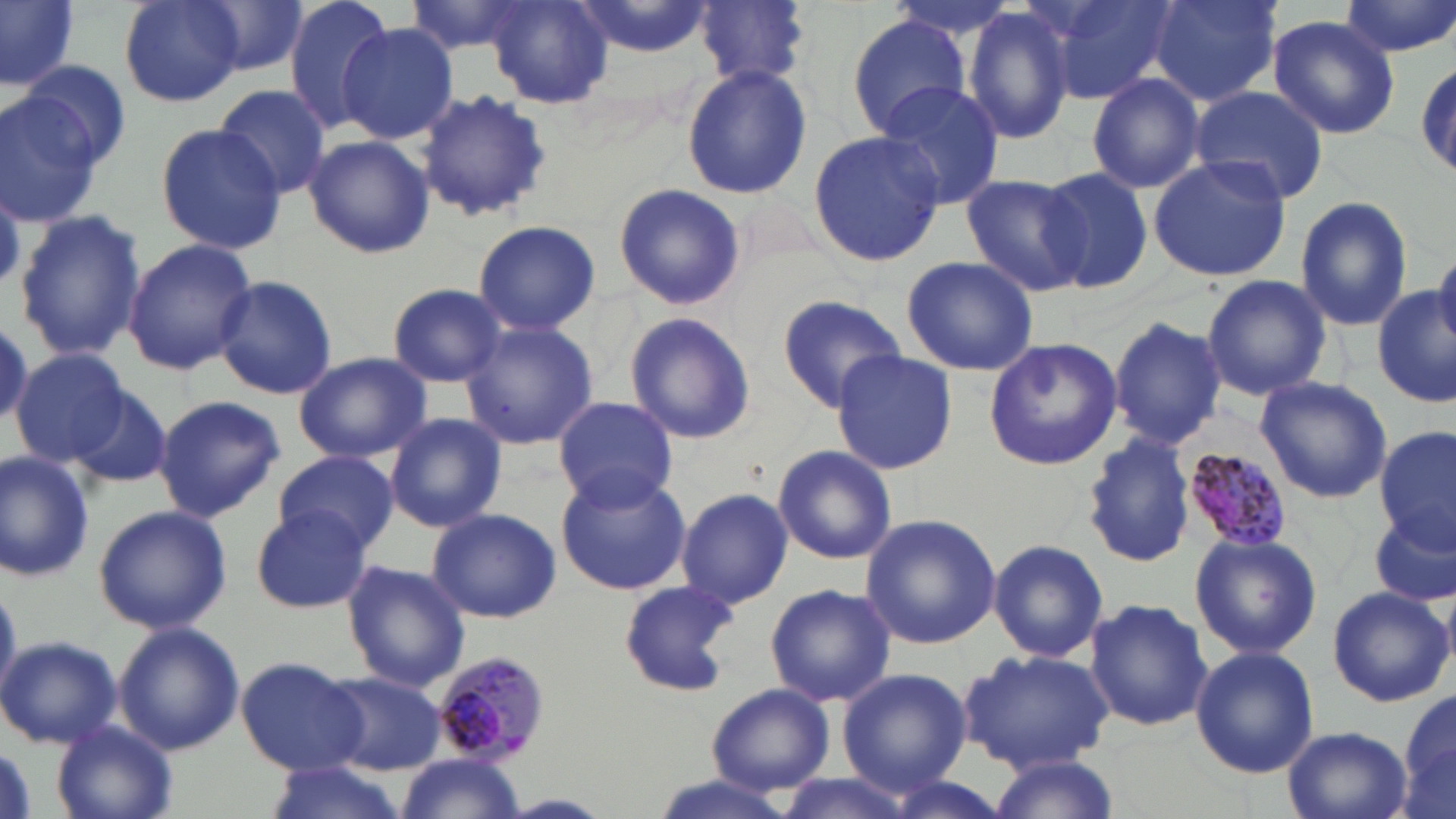
Approximate bounding boxes as (x1,y1)-(x2,y2) corner pairs in pixels. Plasmodium malariae-infected red blood cell locations: (1183,447)-(1293,553), (427,648)-(552,764). Uninfected red blood cell locations: (0,0)-(80,94), (117,0)-(247,107), (191,0)-(314,81), (281,0)-(401,133), (403,0)-(536,56), (572,0)-(715,59), (1043,0)-(1175,103), (1149,0)-(1281,105), (1339,0)-(1455,59), (485,1)-(612,106), (697,1)-(808,87), (964,8)-(1077,145), (845,14)-(971,138), (1268,14)-(1401,139), (335,24)-(460,144), (1415,59)-(1455,183), (18,60)-(134,169), (682,63)-(811,199), (1086,72)-(1206,194), (875,82)-(1006,210), (213,84)-(333,200), (1190,85)-(1329,204), (417,88)-(551,222), (0,90)-(108,228), (154,123)-(287,253), (807,129)-(946,269), (302,135)-(435,260), (1147,155)-(1292,281), (1037,166)-(1156,290), (959,175)-(1090,296), (613,182)-(746,311), (1295,196)-(1412,331), (14,209)-(147,364), (472,219)-(602,335), (123,238)-(257,375), (1432,252)-(1456,350), (901,255)-(1038,376), (1201,273)-(1331,399), (214,276)-(337,399), (385,282)-(507,387), (1373,285)-(1454,409), (775,294)-(910,410), (623,311)-(758,443), (1107,313)-(1226,449), (0,316)-(32,433), (462,320)-(598,451), (982,338)-(1122,472), (10,348)-(129,466), (293,350)-(433,462), (832,350)-(956,474), (1254,376)-(1393,503), (62,382)-(174,489), (153,395)-(285,521), (550,395)-(680,511), (385,413)-(506,531), (1376,429)-(1454,547), (1080,433)-(1199,570), (772,444)-(898,566), (0,449)-(96,581), (276,451)-(400,554), (554,470)-(692,596), (675,488)-(794,609), (93,504)-(231,634), (250,507)-(376,614), (427,507)-(560,623), (1371,508)-(1456,607), (859,514)-(1001,651), (355,522)-(513,665), (1190,531)-(1320,658), (988,539)-(1109,662), (341,561)-(470,690), (618,581)-(738,696), (764,583)-(895,707), (1326,584)-(1455,707), (1085,598)-(1212,731), (112,621)-(245,755), (0,635)-(122,749), (1190,644)-(1319,778), (960,647)-(1114,772), (236,657)-(368,774), (837,667)-(971,793), (321,670)-(447,774), (706,682)-(836,796), (1394,686)-(1456,819), (48,721)-(178,819), (1279,725)-(1416,819), (983,754)-(1123,819), (396,755)-(527,819), (264,761)-(406,816), (768,773)-(919,819), (873,774)-(1016,819). Slide-level diagnosis: Plasmodium malariae. One field of a larger specimen. Captured at 1000x magnification. Image is 1456×819 pixels. Light microscopy. May-Grünwald-Giemsa-stained preparation. Thin blood film.